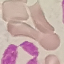

Result: negative for malaria parasites. Acquired by smartphone through the microscope eyepiece. Thin blood film. Automatically extracted cell patch, resized to 64 × 64 pixels. Giemsa-stained preparation.